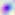

Summary:
  - Identification: Toxoplasma gondii
  - Modality: micrograph
  - Magnification: 400x